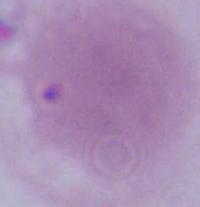
modality: photomicrograph
magnification: 1000x
identification: erythrocyte